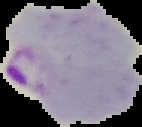 Cell region segmented out of the field of view; the surrounding area is masked to black. Result: malaria parasites identified. From a thin blood film. Image is 142×127 pixels.